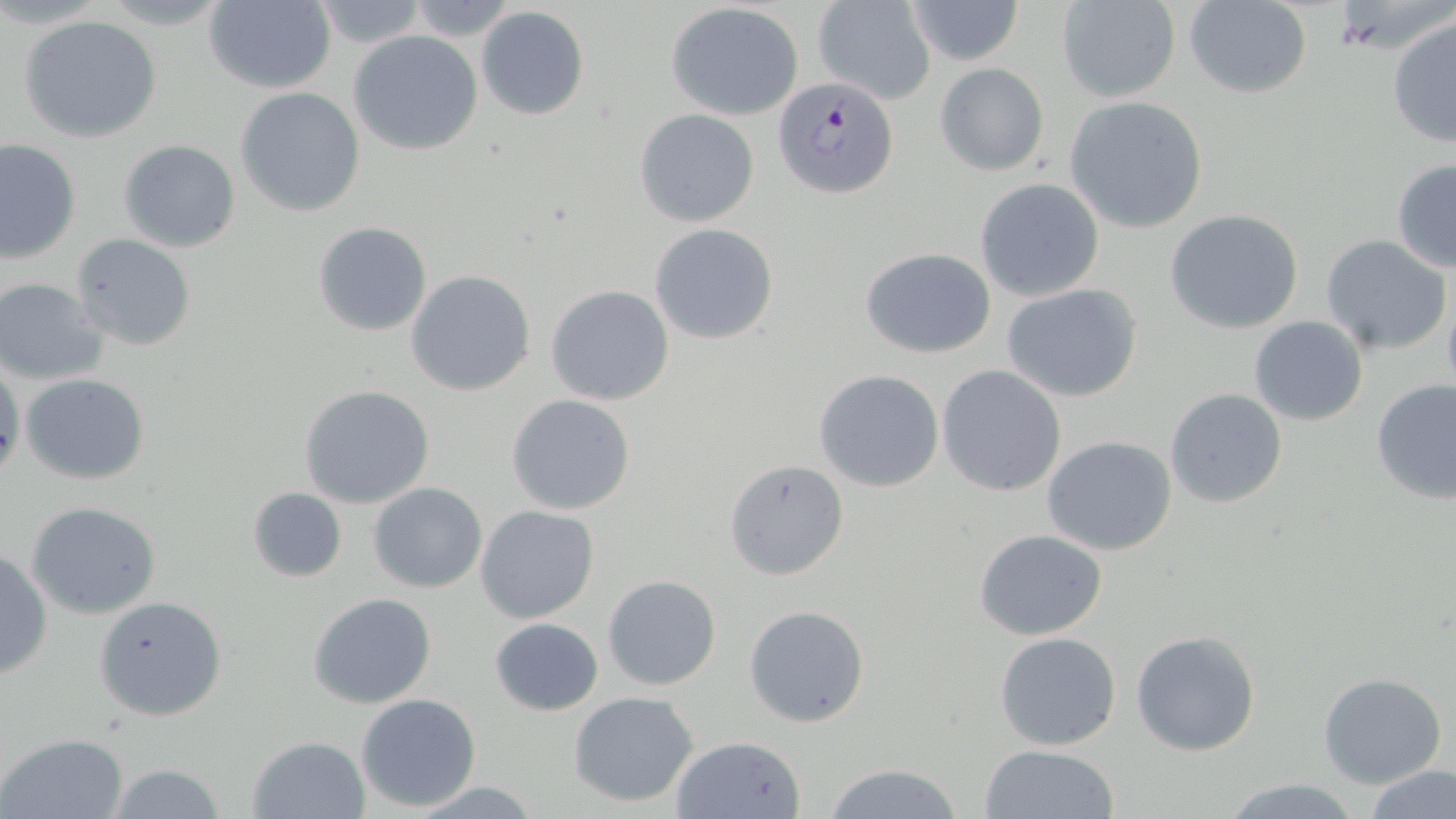
Summary:
  - Coordinate format: approximate bounding boxes as named x1/y1/x2/y2 corners in pixels
  - Plasmodium falciparum-infected red blood cell locations: (x1=773, y1=76, x2=900, y2=201)
  - Uninfected red blood cell locations: (x1=812, y1=0, x2=936, y2=105), (x1=904, y1=0, x2=1024, y2=66), (x1=203, y1=1, x2=337, y2=92), (x1=310, y1=1, x2=430, y2=50), (x1=1182, y1=1, x2=1313, y2=99), (x1=398, y1=2, x2=523, y2=40), (x1=1056, y1=2, x2=1181, y2=104), (x1=666, y1=3, x2=805, y2=118), (x1=476, y1=6, x2=589, y2=120), (x1=1387, y1=12, x2=1456, y2=148), (x1=19, y1=15, x2=163, y2=142), (x1=349, y1=30, x2=483, y2=155), (x1=935, y1=62, x2=1048, y2=176), (x1=235, y1=86, x2=366, y2=216), (x1=1065, y1=95, x2=1209, y2=233), (x1=634, y1=108, x2=760, y2=227), (x1=118, y1=139, x2=241, y2=252), (x1=1, y1=140, x2=78, y2=263), (x1=1390, y1=158, x2=1456, y2=272), (x1=975, y1=178, x2=1104, y2=302), (x1=105, y1=183, x2=229, y2=324), (x1=1165, y1=209, x2=1306, y2=334), (x1=313, y1=222, x2=433, y2=336), (x1=649, y1=224, x2=779, y2=345), (x1=71, y1=233, x2=196, y2=352), (x1=1320, y1=234, x2=1452, y2=355), (x1=860, y1=247, x2=996, y2=357), (x1=405, y1=270, x2=535, y2=397), (x1=1, y1=278, x2=110, y2=383), (x1=545, y1=284, x2=674, y2=406), (x1=1002, y1=284, x2=1144, y2=402), (x1=1442, y1=289, x2=1456, y2=401), (x1=1247, y1=314, x2=1369, y2=426), (x1=0, y1=357, x2=23, y2=483), (x1=937, y1=365, x2=1067, y2=497), (x1=814, y1=370, x2=944, y2=492), (x1=21, y1=373, x2=151, y2=485), (x1=1371, y1=377, x2=1455, y2=504), (x1=298, y1=383, x2=434, y2=508), (x1=1165, y1=388, x2=1288, y2=510), (x1=506, y1=394, x2=635, y2=515), (x1=1043, y1=436, x2=1177, y2=556), (x1=724, y1=458, x2=850, y2=581), (x1=369, y1=482, x2=488, y2=593), (x1=247, y1=486, x2=346, y2=581), (x1=26, y1=500, x2=162, y2=619), (x1=475, y1=505, x2=599, y2=623), (x1=974, y1=529, x2=1107, y2=640), (x1=0, y1=550, x2=51, y2=679), (x1=602, y1=573, x2=722, y2=691), (x1=308, y1=593, x2=437, y2=709), (x1=94, y1=596, x2=227, y2=721), (x1=743, y1=604, x2=871, y2=727), (x1=488, y1=617, x2=604, y2=714), (x1=1131, y1=630, x2=1261, y2=757), (x1=994, y1=631, x2=1123, y2=751), (x1=1317, y1=673, x2=1446, y2=790), (x1=569, y1=691, x2=700, y2=808), (x1=355, y1=693, x2=483, y2=811), (x1=2, y1=732, x2=128, y2=818), (x1=247, y1=735, x2=369, y2=817), (x1=668, y1=735, x2=806, y2=819), (x1=978, y1=743, x2=1121, y2=819), (x1=102, y1=761, x2=226, y2=819), (x1=821, y1=762, x2=965, y2=819), (x1=1364, y1=764, x2=1455, y2=819), (x1=1216, y1=776, x2=1366, y2=818), (x1=402, y1=780, x2=546, y2=817)
  - Slide-level diagnosis: Plasmodium falciparum
  - Image size: 1456×819 pixels
  - Magnification: 1000x
  - Modality: light microscopy
  - Preparation: thin blood smear
  - Stain: May-Grünwald-Giemsa
  - Field of view: one of a larger specimen